Name the parasite shown.
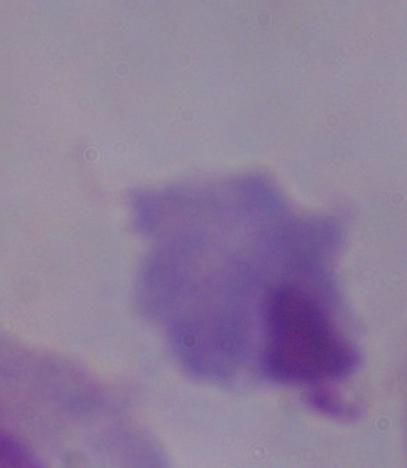
A trichomonad.

magnification = 1000x
modality = photomicrograph